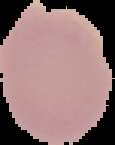 The area outside the segmented cell region is set to black. Result: no Plasmodium parasites seen. From a thin blood film. Image is 115×145 pixels.